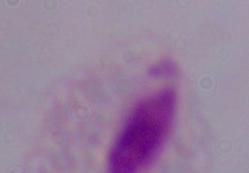

identification = trichomonad
magnification = 1000x
modality = micrograph